Give the preparation type.
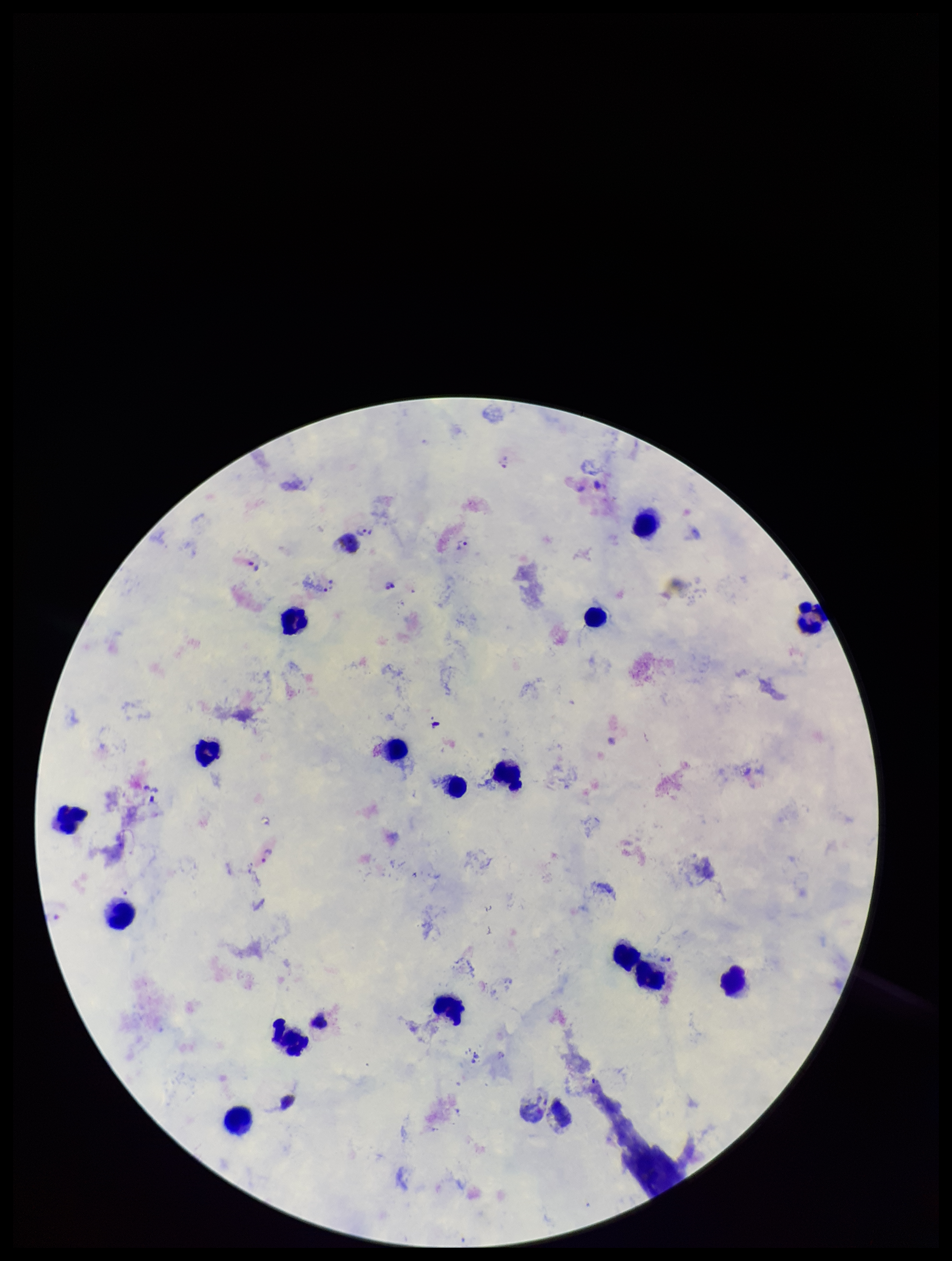

It is a thick blood smear.

Summary:
  - Field of view: one from this slide
  - Parasite count: 6
  - Leukocyte count: 18
  - Patient malaria status: positive
  - Capture: smartphone photograph through the microscope eyepiece
  - Stain: Giemsa
  - Species reported for this patient: Plasmodium vivax
  - Plasmodium parasites: identified
  - Image size: 952×1261 pixels